Identify the parasite.
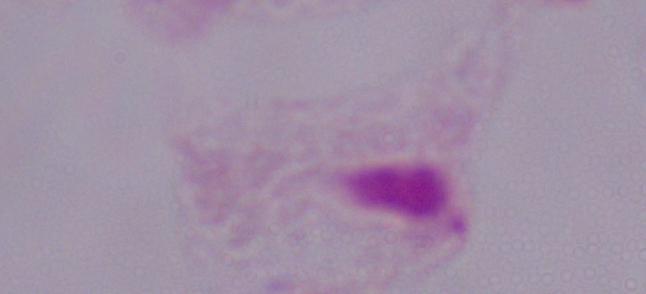
A trichomonad.

Summary:
  - Modality: photomicrograph
  - Magnification: 1000x